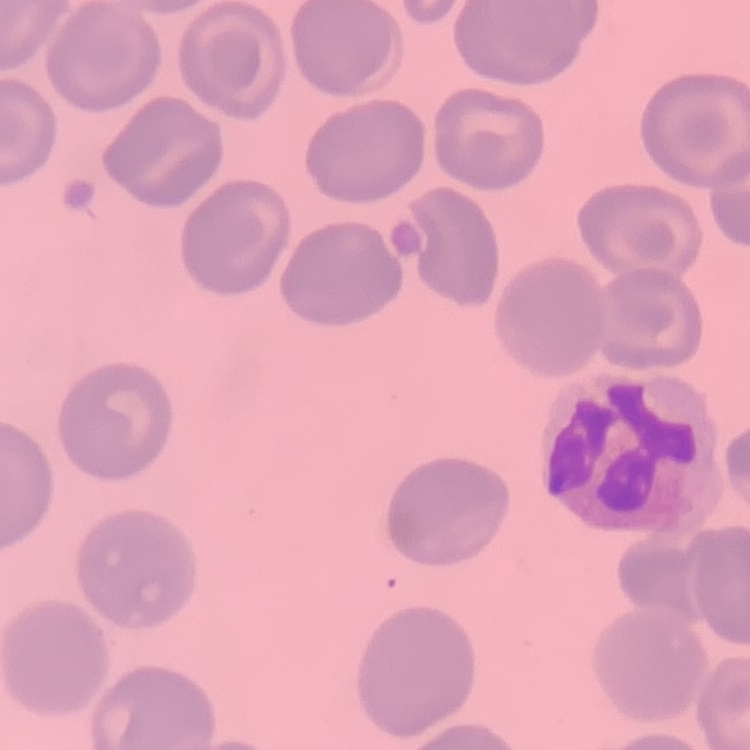

erythrocyte_morphology: no rouleaux formation
preparation: thin peripheral smear
image_type: one tile cut from a larger photomicrograph
stain: Field's or Giemsa